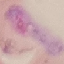

result = malaria parasites identified
capture = smartphone through the microscope eyepiece
stain = Giemsa
image type = cell patch, automatically extracted from a larger field of view and resized to 64 × 64 pixels
preparation = thin smear